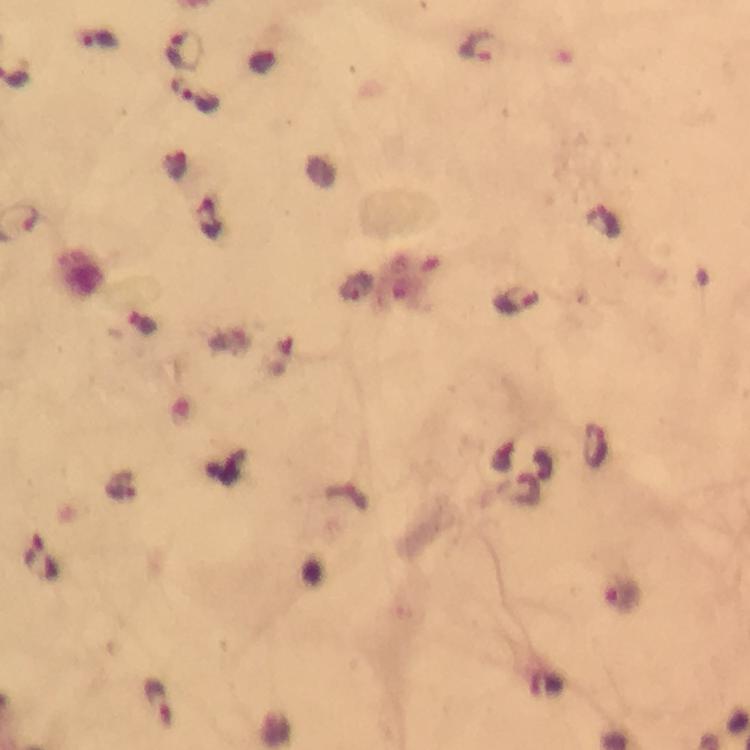

Approximate object centers, in pixels from the top-left corner.
Summary:
  - Plasmodium parasite locations: (x=479, y=48), (x=184, y=51), (x=195, y=94), (x=607, y=222), (x=514, y=301), (x=596, y=447), (x=528, y=490), (x=623, y=595), (x=159, y=701)
  - Stain: Giemsa
  - Capture: smartphone camera through the microscope
  - Magnification: 100x
  - Context: from a diagnostic examination for malaria
  - Cropped from: a single field of view
  - Preparation: thick smear
  - Image size: 750×750 pixels
  - Immersion oil: used